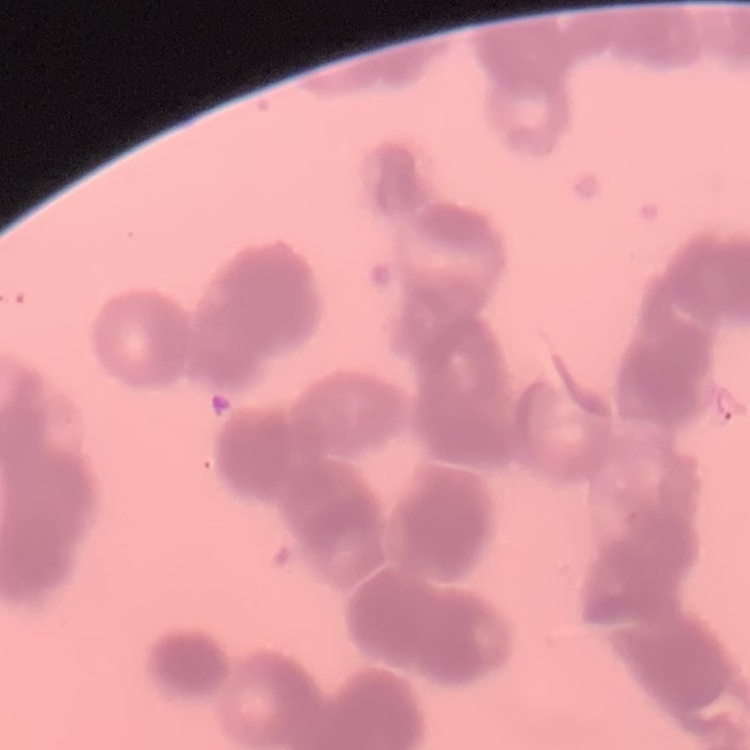
Summary:
  - Red blood cell morphology: rouleaux formation
  - Preparation: thin blood smear
  - Stain: Field's or Giemsa
  - Image type: one tile cut from a larger photomicrograph